Assess this cell for malaria.
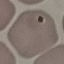

It is uninfected.

image_type: automatically extracted cell patch, resized to 64 × 64 pixels
stain: Giemsa
preparation: thin smear
capture: smartphone through the microscope eyepiece